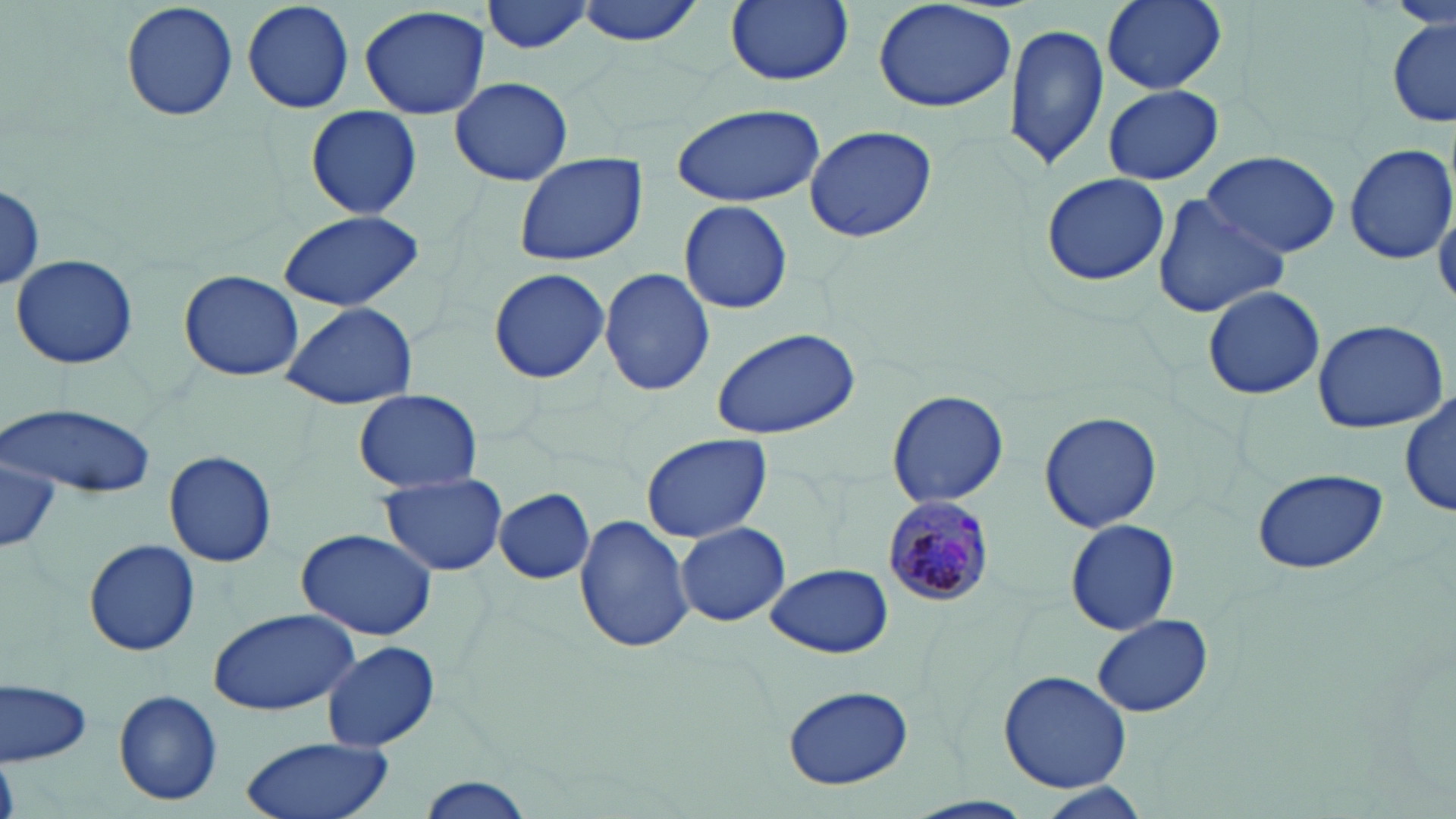

slide-level diagnosis = Plasmodium malariae
preparation = thin blood film
field of view = one of a larger specimen
Plasmodium malariae-infected red blood cell locations = approximate bounding boxes as (x1, y1, x2, y2) in pixels: (881, 495, 992, 610)
stain = May-Grünwald-Giemsa
modality = light microscopy
uninfected red blood cell locations = approximate bounding boxes as (x1, y1, x2, y2) in pixels: (119, 0, 241, 120), (240, 0, 355, 114), (480, 0, 596, 55), (574, 0, 707, 46), (724, 0, 852, 86), (873, 0, 1018, 115), (1099, 0, 1229, 94), (359, 4, 492, 116), (1388, 18, 1455, 126), (1005, 21, 1110, 171), (449, 77, 574, 187), (1104, 84, 1222, 185), (670, 103, 825, 207), (304, 106, 423, 220), (804, 125, 936, 242), (1344, 141, 1455, 265), (1201, 149, 1342, 259), (512, 152, 649, 266), (1040, 172, 1171, 285), (0, 185, 46, 292), (1151, 194, 1291, 317), (1434, 195, 1456, 309), (679, 199, 794, 315), (276, 210, 428, 310), (11, 253, 138, 370), (488, 267, 611, 385), (599, 268, 716, 397), (179, 269, 303, 381), (1203, 285, 1326, 400), (282, 301, 417, 409), (1310, 318, 1450, 435), (709, 326, 861, 438), (354, 390, 481, 493), (885, 390, 1009, 509), (1401, 392, 1454, 520), (2, 402, 154, 499), (1038, 410, 1163, 533), (641, 433, 772, 543), (2, 445, 63, 555), (164, 450, 277, 568), (1248, 467, 1389, 575), (378, 472, 508, 577), (495, 489, 594, 584), (572, 515, 692, 654), (1065, 519, 1178, 635), (675, 522, 790, 627), (296, 527, 439, 640), (83, 537, 201, 657), (767, 563, 893, 658), (207, 607, 361, 717), (1093, 615, 1214, 718), (321, 640, 441, 752), (998, 669, 1132, 790), (0, 677, 93, 767), (780, 684, 915, 791), (113, 690, 221, 806), (240, 735, 397, 819), (418, 776, 536, 819), (1026, 782, 1153, 818)
magnification = 1000x
image size = 1456×819 pixels